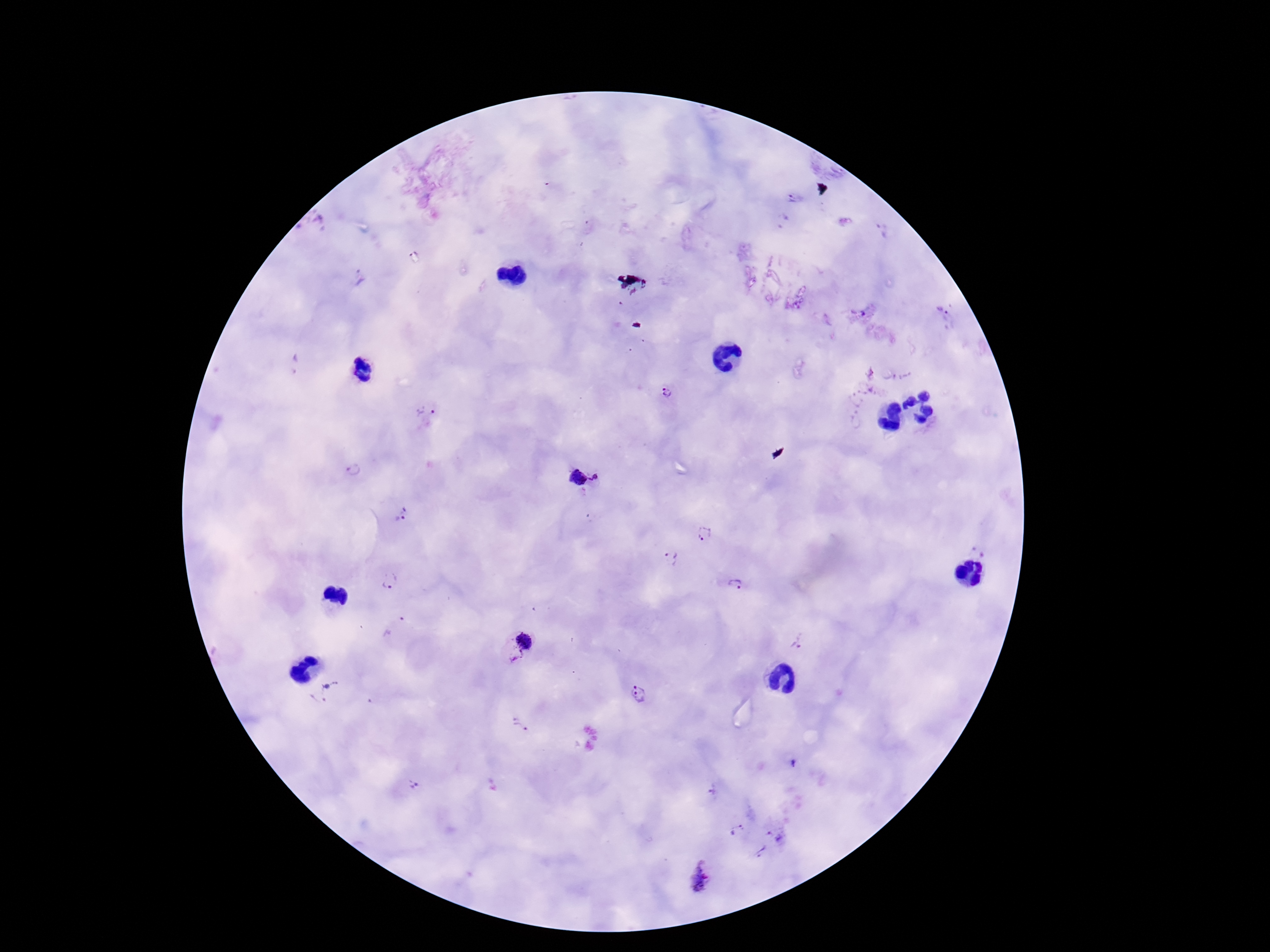

Approximate centers as [x, y] in pixels.
Summary:
  - Plasmodium parasite locations: [796, 198], [881, 229], [359, 277], [942, 311], [667, 392], [428, 416], [353, 471], [598, 476], [576, 478], [401, 514], [704, 534], [671, 558], [392, 582], [735, 584], [797, 640], [519, 644], [326, 693], [638, 695], [522, 725], [793, 763], [413, 786], [713, 790], [739, 829], [777, 833], [760, 851], [701, 876]
  - Preparation: thick blood film
  - Capture: smartphone camera through the microscope eyepiece
  - Image size: 1270×952 pixels
  - Patient malaria status: infected
  - Magnification: 100x
  - Stain: Giemsa
  - Field of view: single